Give the extent of all uninfected red blood cells.
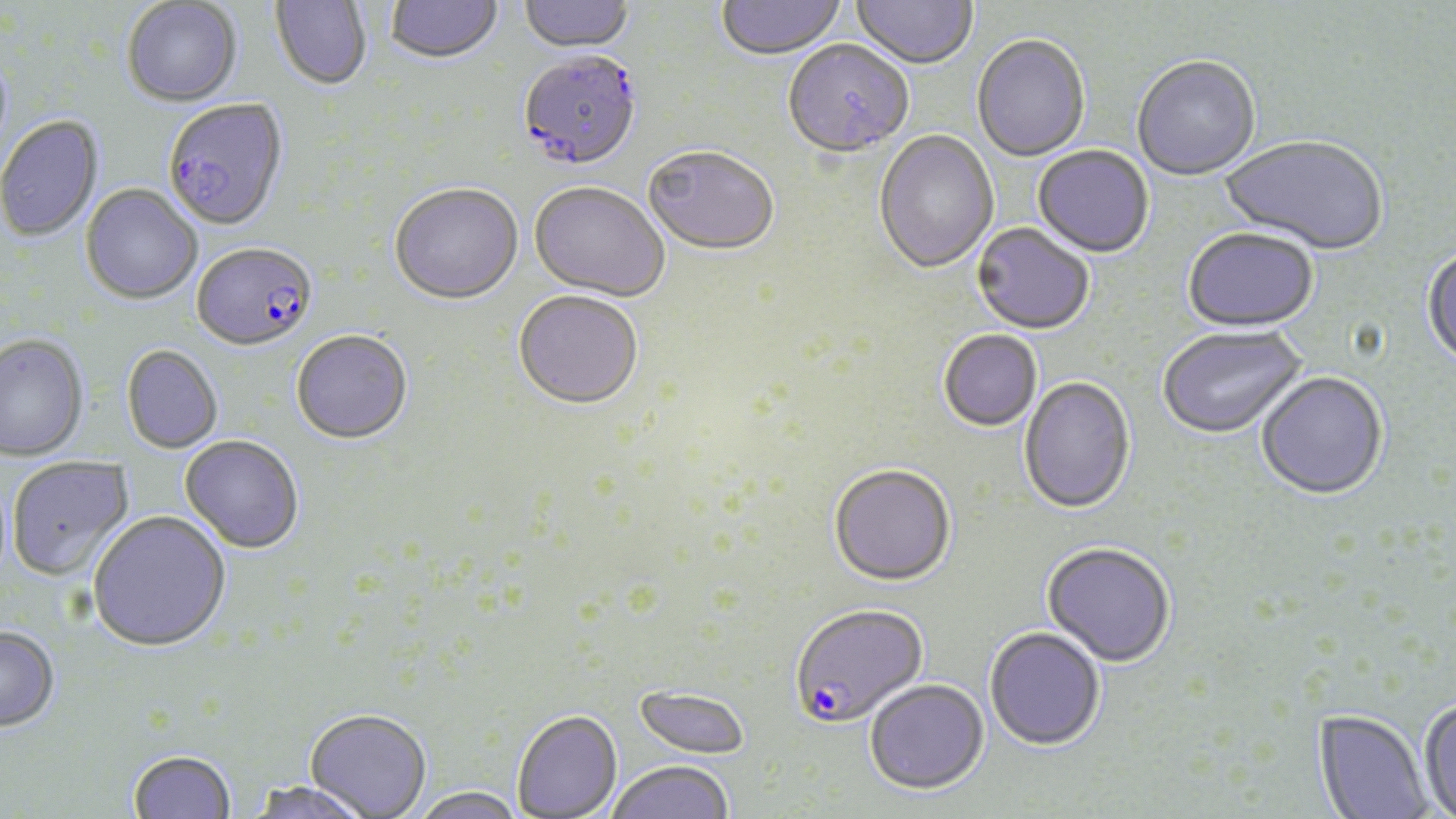
Approximate bounding boxes as (x1,y1)-(x2,y2) corner pairs in pixels.
Uninfected red blood cells: (271,0)-(372,92), (386,0)-(503,67), (519,0)-(635,56), (715,0)-(847,62), (850,0)-(977,72), (122,1)-(242,108), (972,36)-(1090,163), (783,42)-(913,160), (1132,57)-(1261,183), (0,116)-(103,243), (874,131)-(998,276), (1219,137)-(1387,258), (1032,146)-(1154,259), (643,148)-(779,259), (529,184)-(669,304), (80,185)-(202,306), (389,186)-(523,307), (971,224)-(1094,336), (1182,230)-(1319,334), (1422,246)-(1456,371), (513,293)-(643,413), (1158,327)-(1307,440), (938,331)-(1042,433), (291,332)-(413,446), (0,335)-(89,463), (121,346)-(223,454), (1256,373)-(1388,501), (1019,378)-(1136,516), (179,436)-(304,555), (6,456)-(135,582), (828,466)-(956,588), (88,512)-(231,654), (1041,543)-(1175,669), (0,627)-(60,734), (984,628)-(1105,752), (865,680)-(989,795), (633,684)-(751,760), (1417,698)-(1456,819), (304,709)-(431,818), (512,709)-(622,818), (1314,709)-(1431,819), (128,751)-(237,819), (606,760)-(735,819), (246,781)-(373,819), (411,786)-(523,819).

Plasmodium falciparum-infected red blood cell locations: (517,54)-(644,174), (163,100)-(289,234), (191,243)-(318,355), (789,605)-(929,730). Slide-level diagnosis: Plasmodium falciparum. Image is 1456×819 pixels. Thin blood film. Optical microscopy. Captured at 1000x magnification. One field of a larger specimen. May-Grünwald-Giemsa stain.